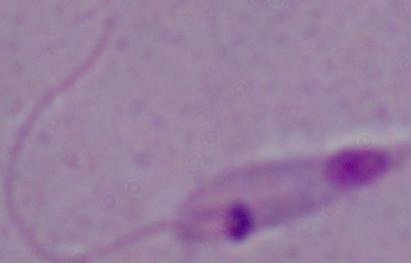

identification = Leishmania
modality = photomicrograph
magnification = 1000x